Assess this cell for malaria.
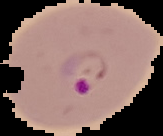

It is parasitized.

Image is 163×136 pixels. Cell region segmented out of the field of view; the surrounding area is masked to black. From a thin blood film.